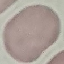
Summary:
  - Result: negative for malaria parasites
  - Stain: Giemsa
  - Image type: cell patch, automatically extracted from a larger field of view and resized to 64 × 64 pixels
  - Capture: smartphone camera at the microscope eyepiece
  - Preparation: thin blood smear